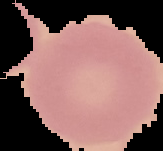

result = no malaria parasites detected
image size = 163×151 pixels
preparation = thin blood smear
image type = segmented cell region with the area outside set to black